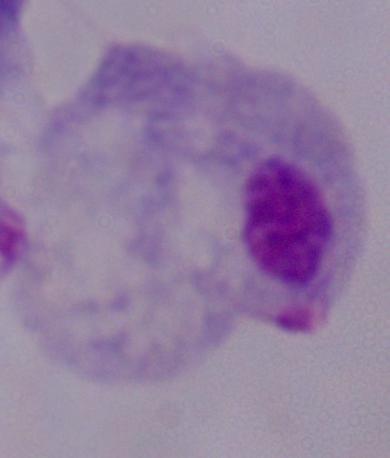 1000x magnification. A trichomonad is seen. Photomicrograph.